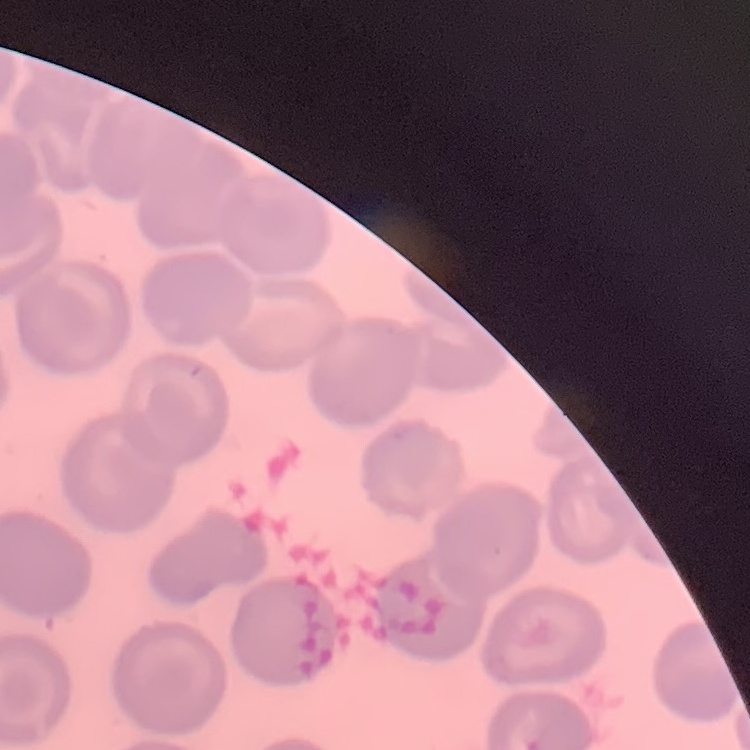
The erythrocytes show no rouleaux formation. Thin peripheral smear. Field's or Giemsa stain. One tile cut from a larger photomicrograph.